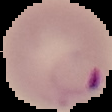

Summary:
  - Image type: segmented cell region with the area outside set to black
  - Image size: 112×112 pixels
  - Malaria status: parasitized
  - Preparation: thin blood film